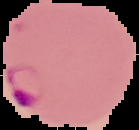
{
  "image_type": "cell region segmented out of the field of view; surrounding area masked to black",
  "preparation": "thin blood smear",
  "result": "malaria parasites identified",
  "image_size": "139×130 pixels"
}